Locate every Plasmodium falciparum-infected red blood cell.
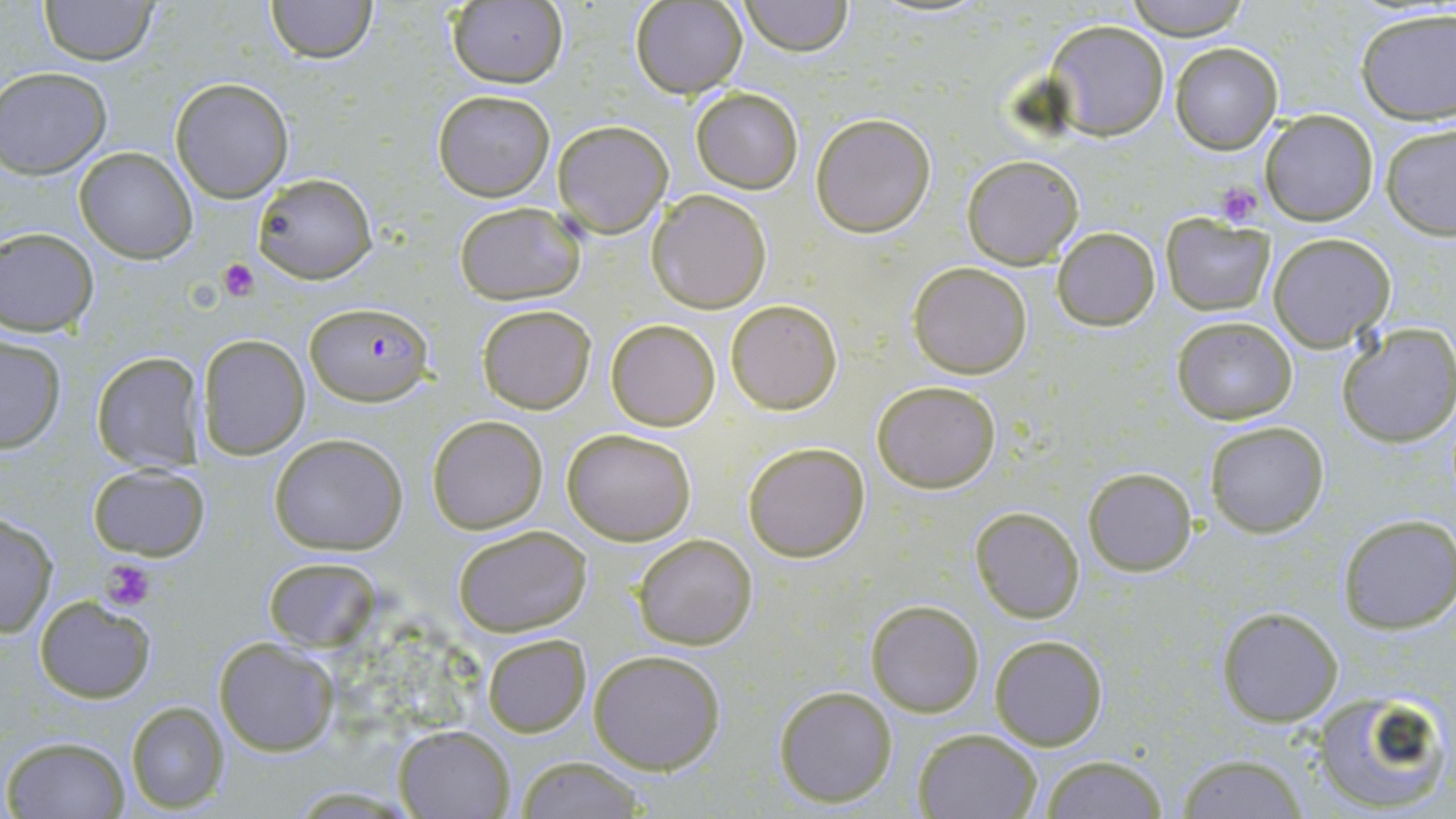

Approximate bounding boxes as named x1/y1/x2/y2 corners in pixels.
Plasmodium falciparum-infected red blood cells: (x1=306, y1=303, x2=433, y2=408).

Summary:
  - Platelet locations: (x1=1212, y1=181, x2=1265, y2=227), (x1=219, y1=258, x2=258, y2=302), (x1=102, y1=558, x2=156, y2=612)
  - Uninfected red blood cell locations: (x1=38, y1=0, x2=158, y2=65), (x1=264, y1=0, x2=379, y2=64), (x1=1121, y1=0, x2=1254, y2=41), (x1=444, y1=1, x2=569, y2=88), (x1=630, y1=1, x2=747, y2=98), (x1=738, y1=1, x2=853, y2=55), (x1=1355, y1=7, x2=1455, y2=124), (x1=1044, y1=19, x2=1170, y2=141), (x1=1170, y1=42, x2=1283, y2=154), (x1=0, y1=67, x2=112, y2=177), (x1=169, y1=80, x2=293, y2=201), (x1=691, y1=87, x2=802, y2=193), (x1=432, y1=90, x2=556, y2=202), (x1=1259, y1=111, x2=1379, y2=225), (x1=810, y1=113, x2=937, y2=238), (x1=551, y1=120, x2=672, y2=238), (x1=1380, y1=123, x2=1455, y2=239), (x1=74, y1=147, x2=198, y2=262), (x1=962, y1=155, x2=1084, y2=269), (x1=252, y1=172, x2=378, y2=285), (x1=648, y1=188, x2=772, y2=313), (x1=453, y1=201, x2=586, y2=305), (x1=1161, y1=214, x2=1275, y2=314), (x1=0, y1=227, x2=98, y2=335), (x1=1052, y1=227, x2=1160, y2=330), (x1=1268, y1=233, x2=1396, y2=352), (x1=909, y1=261, x2=1033, y2=380), (x1=726, y1=299, x2=842, y2=415), (x1=476, y1=305, x2=595, y2=415), (x1=1170, y1=315, x2=1298, y2=423), (x1=606, y1=319, x2=722, y2=432), (x1=1337, y1=322, x2=1456, y2=448), (x1=198, y1=333, x2=309, y2=460), (x1=0, y1=335, x2=67, y2=452), (x1=91, y1=350, x2=208, y2=470), (x1=871, y1=381, x2=1001, y2=494), (x1=429, y1=415, x2=547, y2=533), (x1=1205, y1=420, x2=1329, y2=537), (x1=561, y1=427, x2=697, y2=546), (x1=269, y1=434, x2=408, y2=555), (x1=741, y1=440, x2=870, y2=563), (x1=89, y1=464, x2=210, y2=561), (x1=1084, y1=467, x2=1197, y2=576), (x1=969, y1=505, x2=1085, y2=623), (x1=1, y1=511, x2=60, y2=639), (x1=1338, y1=514, x2=1456, y2=634), (x1=452, y1=527, x2=592, y2=638), (x1=631, y1=532, x2=758, y2=651), (x1=262, y1=557, x2=380, y2=652), (x1=34, y1=595, x2=156, y2=702), (x1=866, y1=600, x2=984, y2=717), (x1=1216, y1=605, x2=1344, y2=727), (x1=481, y1=635, x2=591, y2=736), (x1=989, y1=635, x2=1108, y2=750), (x1=214, y1=639, x2=338, y2=757), (x1=588, y1=649, x2=727, y2=774), (x1=774, y1=684, x2=897, y2=806), (x1=1311, y1=688, x2=1452, y2=815), (x1=124, y1=701, x2=229, y2=813), (x1=394, y1=725, x2=515, y2=818), (x1=911, y1=727, x2=1043, y2=818), (x1=3, y1=736, x2=130, y2=818), (x1=1174, y1=753, x2=1311, y2=818), (x1=514, y1=755, x2=648, y2=819), (x1=1037, y1=756, x2=1171, y2=818)
  - Slide-level diagnosis: Plasmodium falciparum
  - Magnification: 1000x
  - Image size: 1456×819 pixels
  - Preparation: thin blood film
  - Modality: light microscopy
  - Field of view: single
  - Stain: May-Grünwald-Giemsa